Locate every malaria parasite.
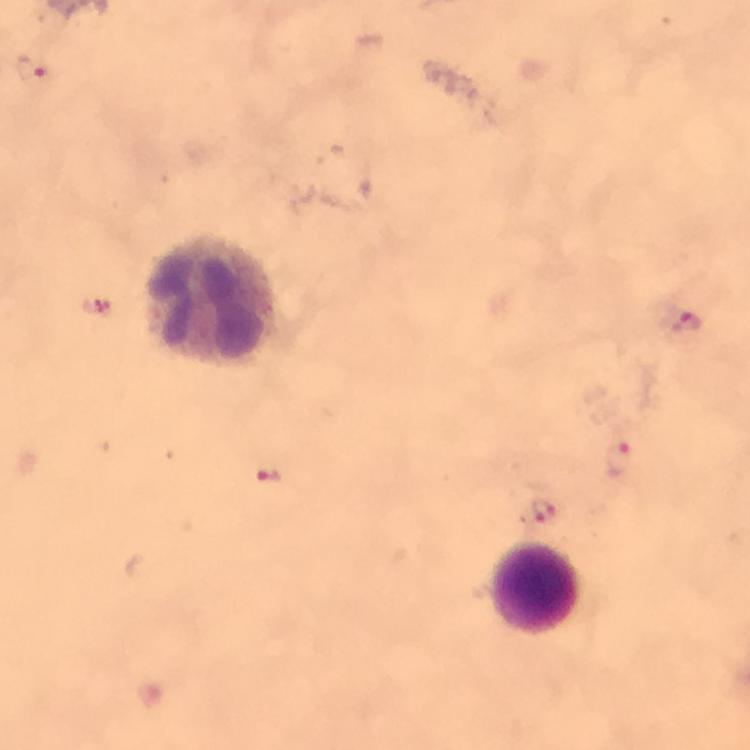

Approximate centers as [x, y] in pixels.
Malaria parasites: [30, 69], [97, 306], [685, 321], [616, 459], [269, 475], [545, 510].

Summary:
  - Leukocyte locations: [210, 297], [535, 587]
  - Magnification: 100x
  - Cropped from: one field of view
  - Immersion oil: applied
  - Preparation: thick blood film
  - Context: from a diagnostic examination for malaria
  - Stain: Giemsa
  - Image size: 750×750 pixels
  - Capture: smartphone photograph through a microscope